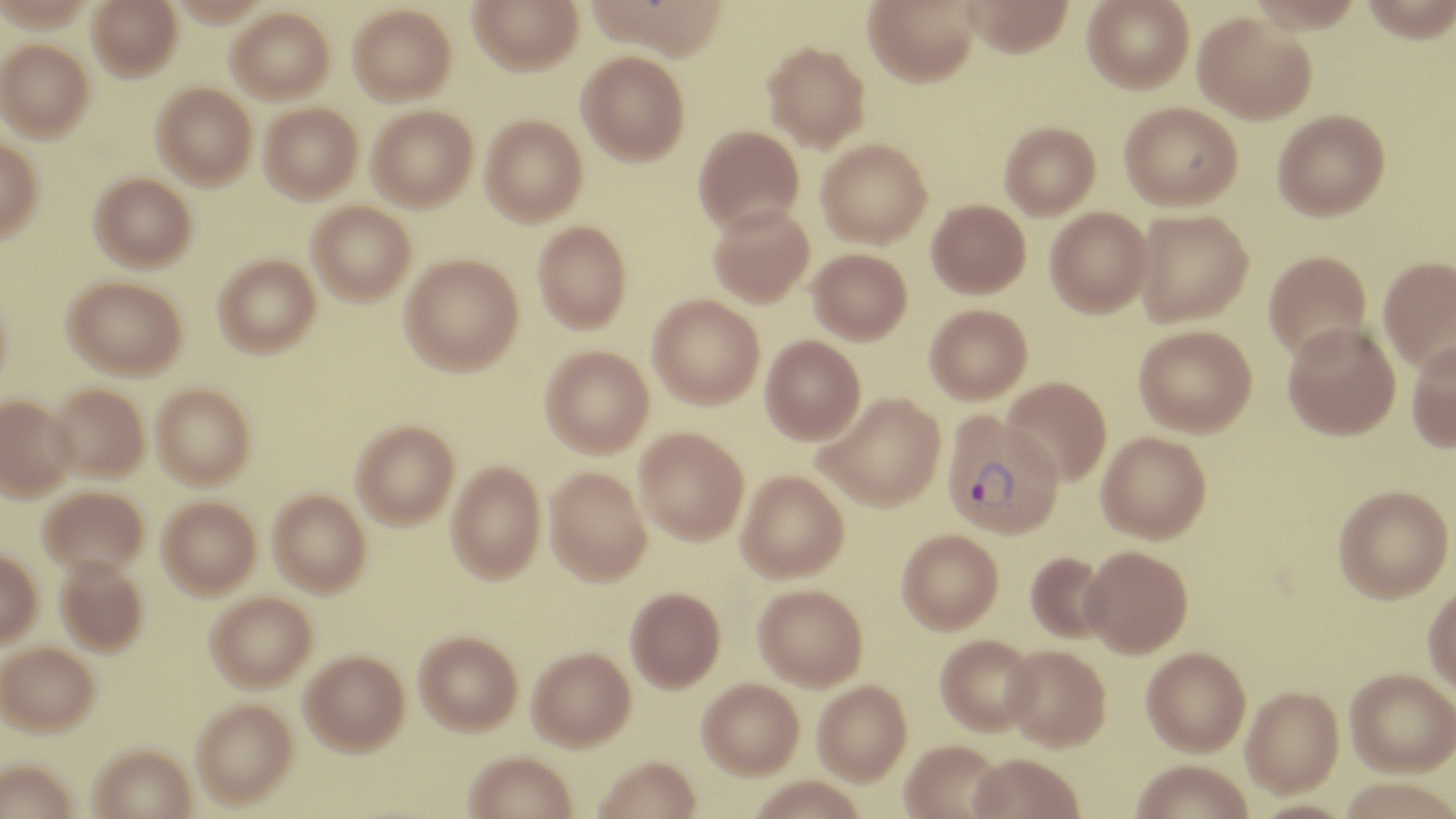
Summary:
  - Coordinate format: approximate bounding boxes as [x1, y1, x2, y2] in pixels
  - Uninfected red blood cell locations: [88, 0, 181, 80], [468, 0, 583, 74], [588, 0, 731, 61], [863, 0, 980, 86], [962, 0, 1074, 57], [1082, 0, 1194, 93], [1245, 0, 1365, 32], [1361, 0, 1456, 44], [347, 4, 456, 104], [227, 7, 334, 103], [1193, 11, 1317, 124], [0, 39, 94, 140], [762, 41, 870, 152], [576, 50, 689, 165], [152, 83, 257, 188], [1119, 101, 1242, 210], [259, 103, 362, 203], [367, 105, 478, 211], [1272, 109, 1390, 221], [480, 114, 587, 226], [1000, 121, 1101, 219], [693, 125, 804, 234], [0, 137, 43, 243], [816, 139, 932, 248], [90, 172, 196, 271], [926, 199, 1030, 298], [307, 201, 416, 304], [708, 205, 814, 307], [1045, 207, 1153, 317], [1134, 210, 1253, 326], [533, 221, 631, 333], [808, 248, 912, 344], [1263, 250, 1372, 362], [400, 253, 523, 375], [213, 254, 321, 357], [1379, 256, 1456, 373], [63, 275, 187, 378], [0, 286, 13, 395], [647, 294, 764, 408], [924, 304, 1032, 403], [1282, 322, 1401, 440], [1134, 325, 1257, 436], [761, 335, 866, 443], [1406, 340, 1456, 452], [540, 345, 653, 457], [1002, 377, 1112, 486], [47, 383, 149, 481], [151, 383, 255, 488], [816, 392, 945, 510], [0, 395, 75, 501], [351, 420, 459, 528], [634, 427, 749, 544], [1097, 431, 1212, 543], [447, 460, 546, 583], [545, 466, 651, 585], [736, 471, 849, 582], [38, 485, 148, 576], [1333, 485, 1454, 602], [268, 489, 371, 595], [158, 495, 261, 597], [897, 529, 1003, 633], [1081, 545, 1193, 657], [0, 549, 41, 646], [1025, 551, 1110, 644], [55, 555, 148, 655], [1423, 582, 1456, 699], [753, 584, 868, 690], [625, 587, 725, 691], [206, 590, 317, 691], [414, 630, 522, 734], [935, 634, 1039, 736], [0, 641, 99, 735], [1003, 644, 1111, 751], [527, 645, 635, 749], [1141, 647, 1251, 756], [301, 649, 409, 754], [1344, 669, 1455, 778], [697, 677, 803, 777], [813, 680, 911, 784], [1241, 687, 1343, 798], [191, 698, 297, 807], [900, 740, 1005, 819], [90, 744, 197, 819], [463, 751, 577, 819], [968, 754, 1084, 819], [594, 756, 701, 819], [1, 758, 77, 819], [1130, 761, 1253, 819], [1337, 778, 1455, 819], [1247, 801, 1358, 819]
  - Plasmodium vivax-infected red blood cell locations: [941, 412, 1065, 539]
  - Slide-level diagnosis: Plasmodium vivax
  - Field of view: single
  - Modality: optical microscopy
  - Magnification: 1000x
  - Stain: May-Grünwald-Giemsa
  - Image size: 1456×819 pixels
  - Preparation: thin blood film